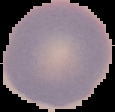
The area outside the segmented cell region is set to black. Result: no Plasmodium parasites detected. Image is 115×112 pixels. From a thin blood film.